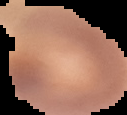 Segmented cell region on a black background. Malaria status: uninfected. From a thin blood film. Image is 127×115 pixels.